Classify this cell by malaria status.
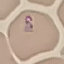
It is parasitized.

{
  "preparation": "thin blood smear",
  "image_type": "automatically extracted cell patch, resized to 64 × 64 pixels",
  "stain": "Giemsa",
  "capture": "smartphone through the microscope eyepiece"
}